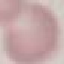 Malaria status: uninfected. Giemsa stain. Photographed with a smartphone camera at the microscope eyepiece. Thin blood film. Automatically extracted cell patch, resized to 64 × 64 pixels.